Classify this cell by malaria status.
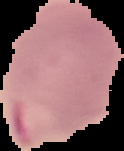
It is parasitized.

{
  "preparation": "thin blood smear",
  "image_type": "cell region segmented out of the field of view; surrounding area masked to black",
  "image_size": "124×151 pixels"
}